Classify this cell by malaria status.
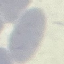
It is uninfected.

Giemsa-stained preparation. Cell patch, automatically extracted from a larger field of view and resized to 64 × 64 pixels. Thin blood film. Photographed with a smartphone camera at the microscope eyepiece.